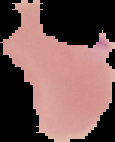
Summary:
  - Image type: cell region segmented out of the field of view; surrounding area masked to black
  - Preparation: thin blood smear
  - Result: Plasmodium parasites detected
  - Image size: 115×142 pixels